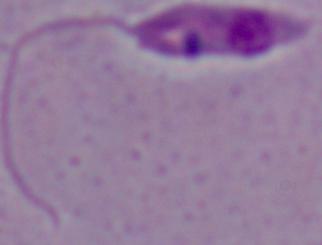

{
  "magnification": "1000x",
  "modality": "micrograph",
  "identification": "Leishmania"
}